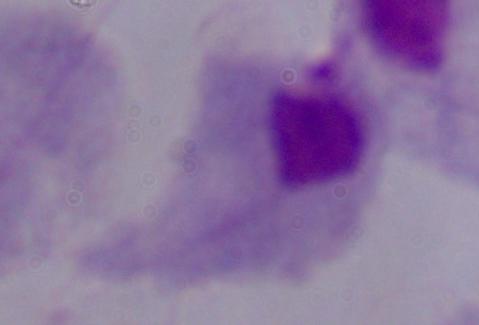

modality: micrograph
identification: trichomonad
magnification: 1000x